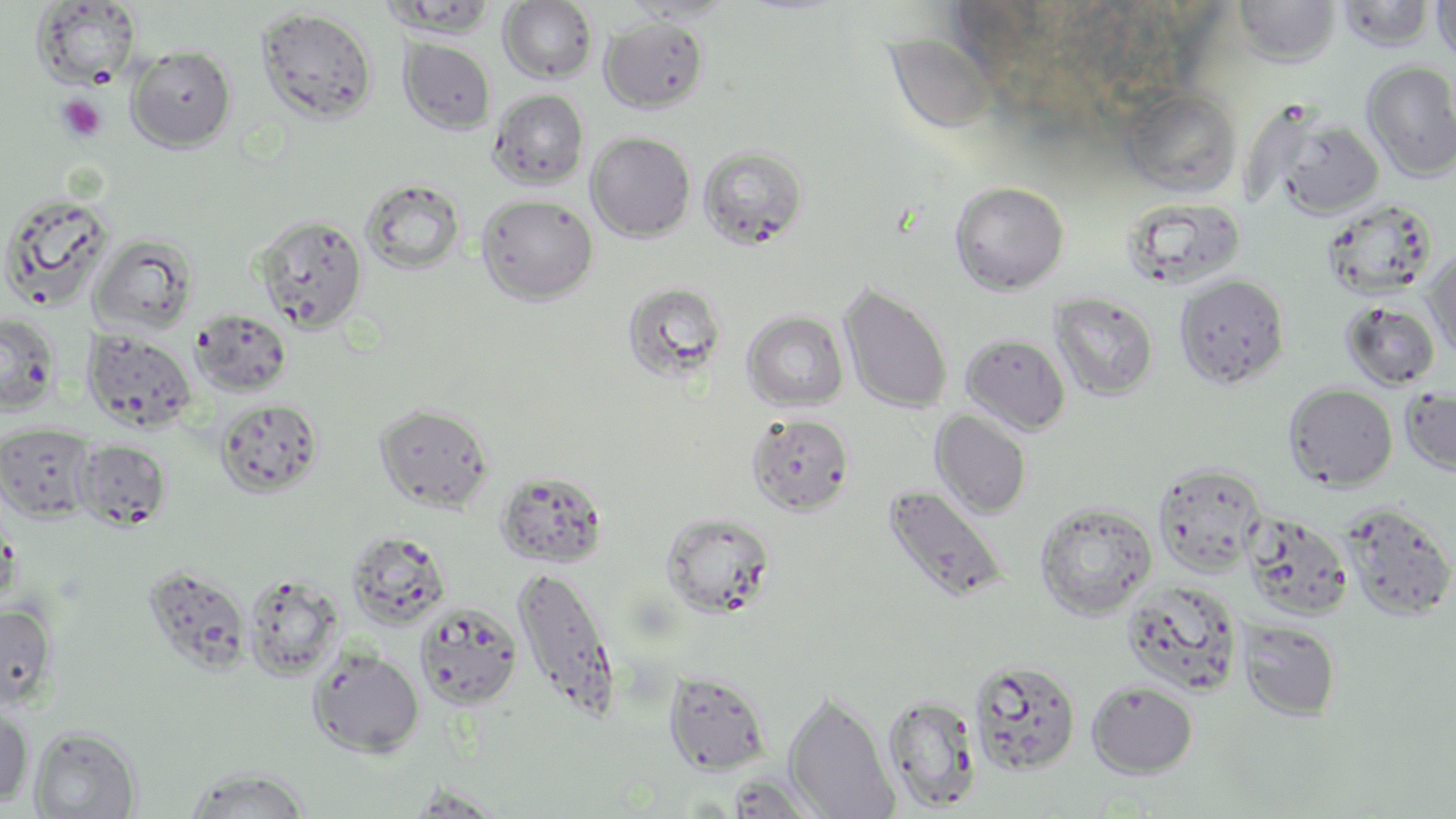

slide-level diagnosis = no evidence of blood parasites
preparation = thin blood smear
field of view = single
uninfected red blood cell locations = approximate bounding boxes as (x1,y1)-(x2,y2) corner pairs in pixels: (621,0)-(736,23), (1233,0)-(1341,68), (32,1)-(142,88), (381,1)-(498,39), (498,1)-(598,84), (1337,1)-(1437,52), (1431,1)-(1456,66), (255,7)-(378,125), (599,15)-(709,114), (887,36)-(997,135), (399,37)-(497,135), (126,45)-(237,151), (1361,61)-(1456,181), (1122,87)-(1242,197), (488,89)-(588,189), (1266,111)-(1387,220), (586,131)-(696,241), (698,144)-(809,251), (361,179)-(466,275), (949,181)-(1069,295), (0,191)-(116,312), (476,193)-(598,305), (1119,196)-(1247,291), (1321,199)-(1437,300), (254,214)-(369,332), (90,233)-(198,336), (1423,247)-(1456,360), (1174,274)-(1290,389), (622,280)-(728,384), (839,283)-(953,414), (1049,292)-(1159,401), (1340,300)-(1441,391), (191,308)-(293,398), (742,311)-(849,412), (0,313)-(61,415), (82,328)-(197,432), (961,334)-(1071,435), (1284,383)-(1397,490), (1400,385)-(1456,476), (215,398)-(324,497), (374,403)-(494,513), (931,410)-(1032,518), (746,413)-(854,516), (0,422)-(96,522), (74,439)-(171,530), (1153,461)-(1267,577), (494,469)-(609,569), (882,484)-(1009,604), (1034,501)-(1158,620), (1341,503)-(1456,622), (661,511)-(776,617), (1242,511)-(1354,621), (345,529)-(451,629), (144,565)-(252,674), (513,565)-(619,719), (243,572)-(344,680), (1120,578)-(1244,696), (414,601)-(523,710), (0,603)-(57,710), (1237,618)-(1341,721), (308,649)-(425,758), (968,658)-(1082,776), (664,670)-(771,775), (1086,679)-(1199,778), (783,692)-(900,819), (881,693)-(983,813), (0,704)-(34,808), (29,726)-(141,818), (183,767)-(312,818), (723,774)-(828,818), (404,786)-(512,817)
magnification = 1000x
modality = optical microscopy
image size = 1456×819 pixels
platelet locations = approximate bounding boxes as (x1,y1)-(x2,y2) corner pairs in pixels: (56,93)-(108,143)
stain = May-Grünwald-Giemsa